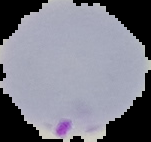
preparation: thin blood film
result: Plasmodium parasites detected
image_size: 151×142 pixels
image_type: segmented cell region with the area outside set to black